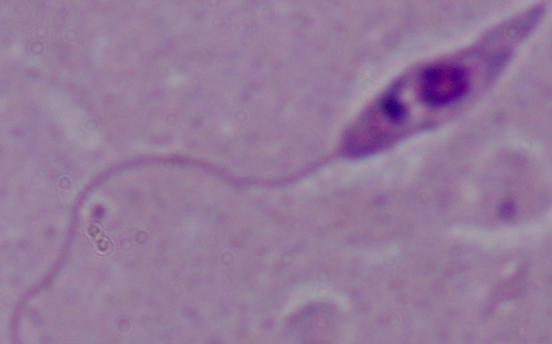
modality = photomicrograph
magnification = 1000x
identification = Leishmania